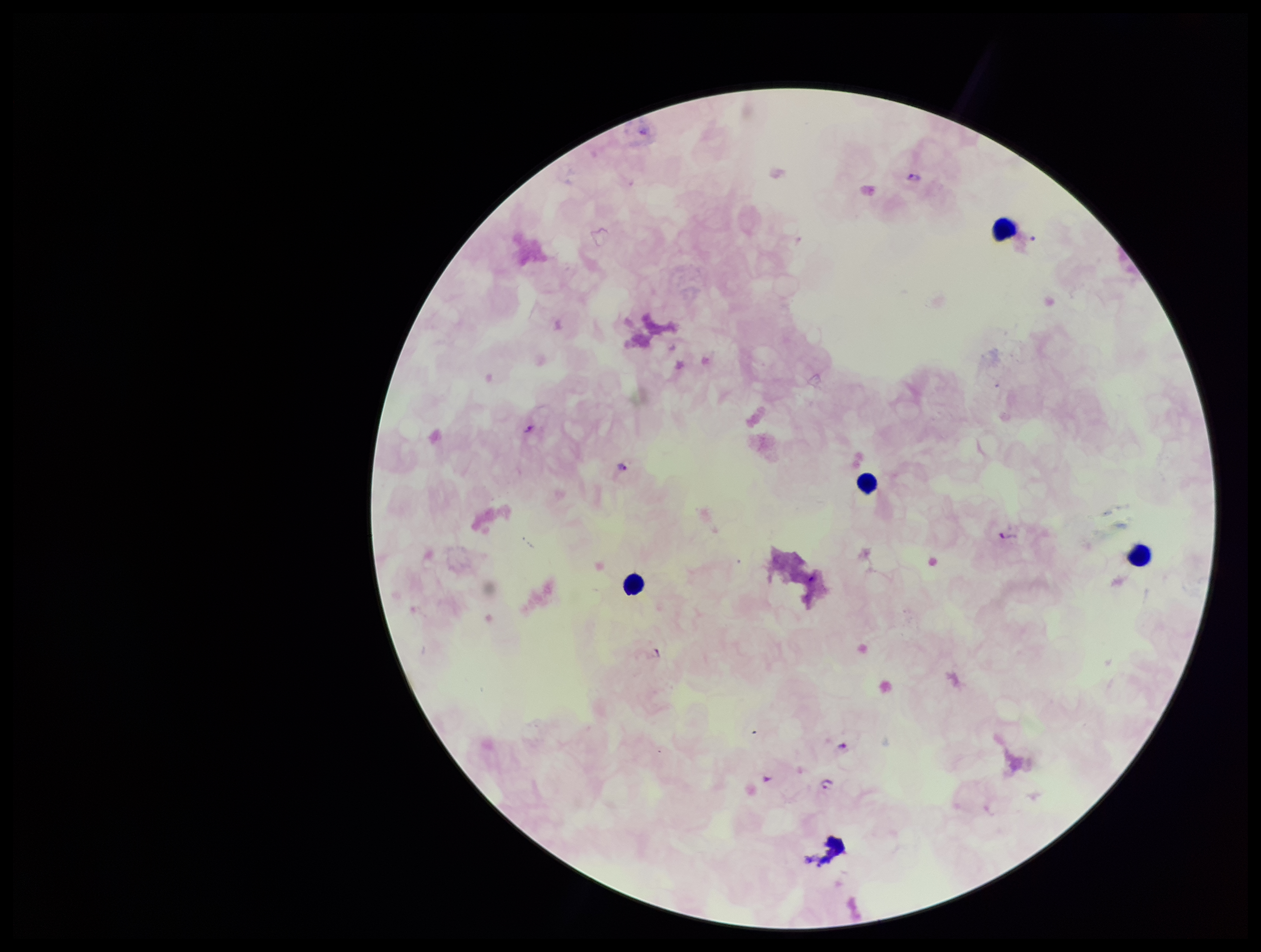

Parasite count: 3. Plasmodium parasites: seen. Image is 1261×952 pixels. Photographed through the microscope eyepiece with a smartphone camera. Patient malaria status: positive. Giemsa stain. Species reported for this patient: Plasmodium falciparum. Preparation: thick smear. Leukocyte count: 4. Single field of view.